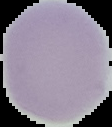
The area outside the segmented cell region is set to black. Malaria status: uninfected. Image is 112×127 pixels. From a thin blood smear.